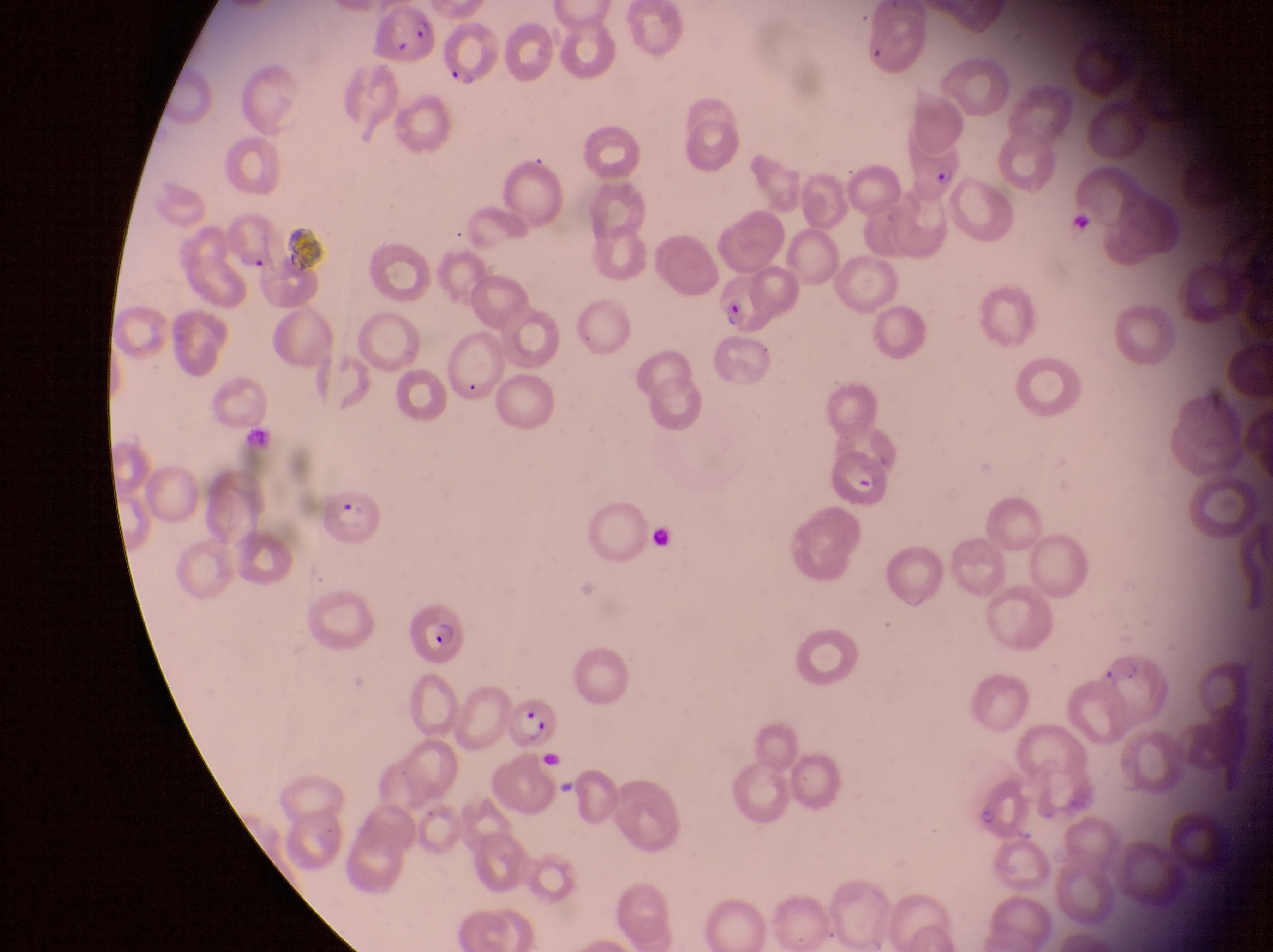
Approximate bounding boxes as left top right bottom in pixels.
Summary:
  - Artifact (platelet-like body, stain precipitate, or debris) locations: 1068 216 1094 239; 647 522 679 556; 554 777 580 800
  - Parasitised red blood cell locations: 375 9 438 66; 904 150 966 203; 222 213 282 271; 720 275 776 336; 829 442 892 517; 322 491 384 549; 409 605 478 675; 1098 647 1172 725; 512 694 565 754; 968 786 1026 848
  - Image size: 1273×952 pixels
  - Capture: smartphone photograph through the eyepiece of an Olympus CX-23 microscope
  - Preparation: thin blood film
  - Field of view: single
  - Country: Uganda
  - Magnification: 1000x